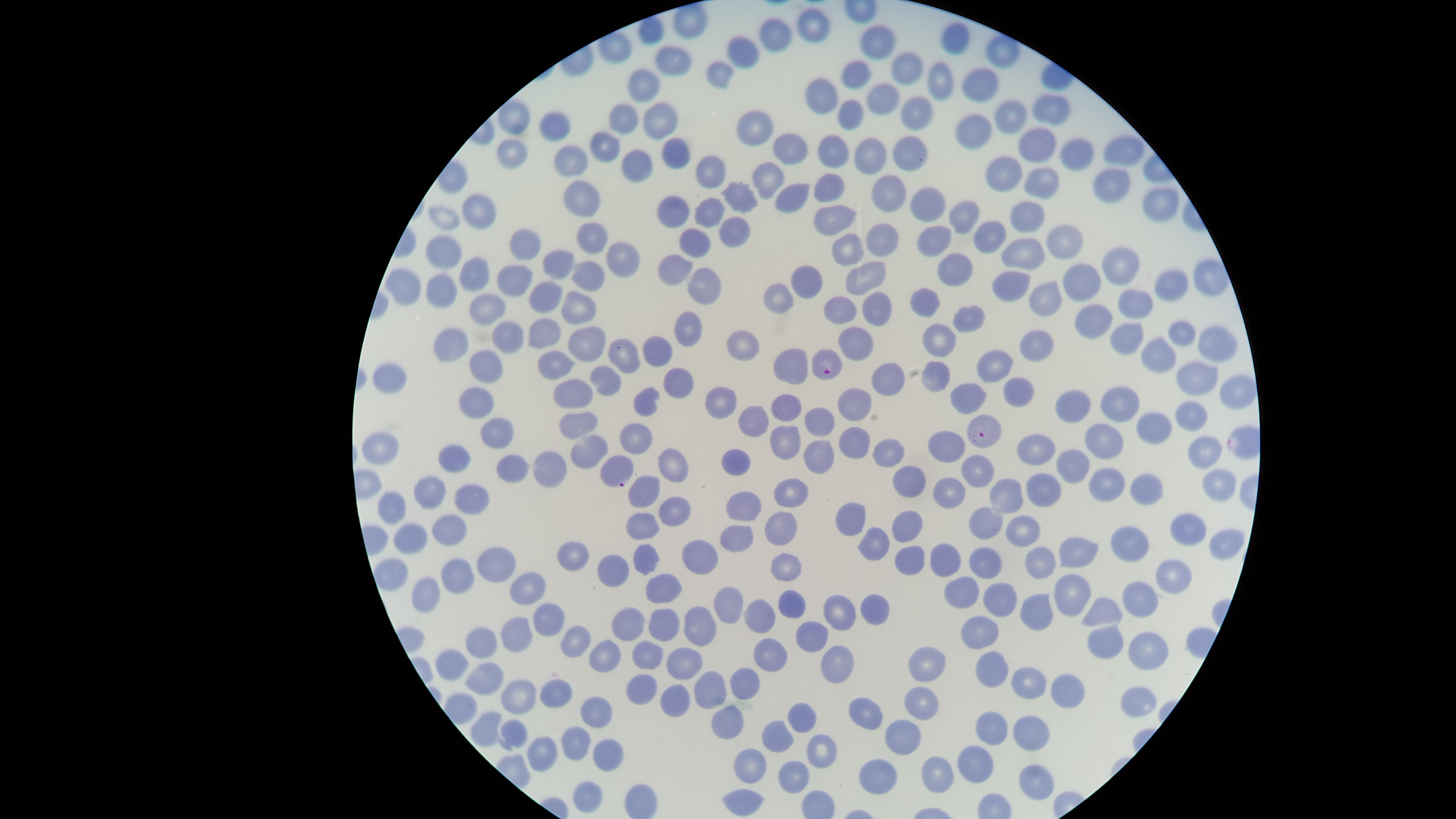

Approximate marker points as (x, y) in pixels.
Summary:
  - Parasitized red blood cells: (825, 362), (987, 434), (619, 464)
  - Uninfected red blood cells: (688, 24), (816, 25), (650, 33), (778, 37), (956, 38), (885, 43), (752, 46), (1003, 52), (676, 53), (914, 66), (721, 75), (860, 76), (941, 78), (647, 81), (981, 86), (826, 88), (877, 100), (1052, 107), (910, 110), (851, 111), (661, 113), (1010, 115), (624, 116), (511, 119), (553, 125), (752, 126), (976, 136), (787, 141), (835, 143), (604, 144), (670, 145), (1038, 147), (1119, 150), (506, 151), (906, 152), (868, 153), (1076, 155), (570, 160), (631, 168), (710, 171), (766, 177), (1003, 177), (1037, 181), (832, 186), (1106, 187), (886, 193), (787, 194), (585, 195), (746, 196), (676, 203), (926, 204), (1156, 206), (711, 212), (830, 216), (481, 219), (1026, 219), (967, 220), (454, 223), (730, 225), (596, 235), (994, 236), (1058, 237), (882, 239), (928, 241), (449, 244), (527, 244), (696, 244), (847, 244), (1018, 256), (627, 259), (564, 260), (1122, 265), (676, 269), (960, 269), (476, 271), (596, 271), (864, 274), (513, 276), (1084, 279), (443, 281), (809, 281), (1014, 283), (1199, 285), (707, 286), (1167, 286), (410, 288), (1046, 292), (546, 297), (918, 298), (779, 299), (488, 302), (1132, 303), (840, 306), (583, 309), (869, 309), (1094, 320), (970, 321), (696, 325), (545, 330), (503, 334), (1182, 334), (941, 336), (1125, 338), (852, 342), (1040, 342), (454, 343), (1215, 344), (589, 345), (746, 345), (655, 347), (622, 356), (557, 360), (1155, 360), (994, 363), (778, 364), (484, 366), (608, 372), (935, 372), (886, 374), (396, 375), (1194, 379), (682, 382), (1018, 384), (573, 388), (1234, 390), (966, 394), (479, 401), (648, 401), (720, 401), (864, 401), (1072, 401), (1118, 401), (786, 407), (1190, 411), (577, 418), (752, 419), (826, 420), (1158, 424), (500, 430), (627, 433), (1109, 437), (785, 439), (945, 439), (857, 443), (590, 444), (383, 449), (819, 449), (1199, 450), (1043, 451), (890, 453), (1073, 459), (454, 460), (739, 462), (518, 465), (675, 465), (977, 466), (551, 468), (909, 481), (435, 483), (1044, 484), (1209, 484), (647, 486), (1113, 486), (1138, 491), (947, 493), (788, 495), (473, 496), (1007, 496), (394, 502), (673, 506), (745, 513), (862, 518), (443, 526), (642, 527), (907, 527), (984, 527), (781, 530), (1182, 530), (1024, 532), (737, 535), (413, 538), (879, 541), (1132, 546), (1222, 546), (1094, 548), (570, 552), (648, 554), (695, 557), (913, 558), (946, 558), (1046, 559), (986, 561), (495, 563), (788, 567), (392, 570), (611, 572), (452, 573), (1174, 573), (528, 585), (659, 585), (424, 590), (963, 592), (1074, 593), (735, 599), (1138, 600), (789, 602), (1000, 602), (1036, 605), (872, 608), (1104, 608), (547, 615), (838, 615), (759, 617), (700, 621), (622, 624), (660, 626), (815, 632), (510, 635), (979, 635), (577, 638), (1109, 639), (478, 640), (770, 651), (608, 652), (1150, 653), (644, 654), (455, 656), (686, 658), (832, 660), (925, 661), (998, 671), (485, 672), (712, 683), (748, 683), (1028, 684), (642, 685), (1071, 693), (510, 695), (918, 695), (561, 696), (679, 696), (1133, 700), (602, 708), (865, 714), (719, 718), (800, 719), (992, 725), (481, 727), (1031, 727), (513, 733), (775, 735), (904, 737), (575, 746), (822, 746), (543, 750), (605, 752), (750, 756), (975, 762), (794, 773), (942, 773), (874, 775), (1033, 781), (587, 795), (741, 800)
  - Field of view: single
  - Species: Plasmodium falciparum
  - Capture: smartphone photograph through the microscope eyepiece
  - Image size: 1456×819 pixels
  - Preparation: thin blood film
  - Presence: malaria parasites detected
  - Visible region: circular
  - Stain: Giemsa